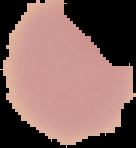

From a thin blood smear. Malaria status: uninfected. Image is 136×148 pixels. The area outside the segmented cell region is set to black.